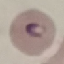
Result: malaria parasites identified. Giemsa stain. Acquired by smartphone through the microscope eyepiece. Cell patch, automatically extracted from a larger field of view and resized to 64 × 64 pixels. Thin smear of blood.